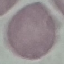 Result: negative for malaria parasites. Thin blood film. Automatically extracted cell patch, resized to 64 × 64 pixels. Photographed with a smartphone camera at the microscope eyepiece. Giemsa stain.